Report the malaria status of this cell.
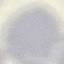
Uninfected.

Summary:
  - Stain: Giemsa
  - Image type: cell patch, automatically extracted from a larger field of view and resized to 64 × 64 pixels
  - Capture: smartphone camera at the microscope eyepiece
  - Preparation: thin blood film